Identify the cell.
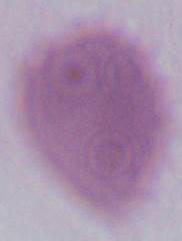
This is an erythrocyte.

modality = micrograph
magnification = 1000x